Report the malaria status of this cell.
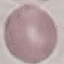

It is uninfected.

stain = Giemsa
image type = automatically extracted cell patch, resized to 64 × 64 pixels
preparation = thin blood film
capture = smartphone through the microscope eyepiece